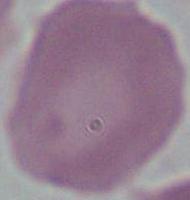
magnification = 1000x
modality = photomicrograph
identification = red blood cell